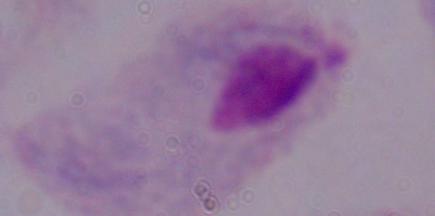

{
  "magnification": "1000x",
  "identification": "trichomonad",
  "modality": "photomicrograph"
}